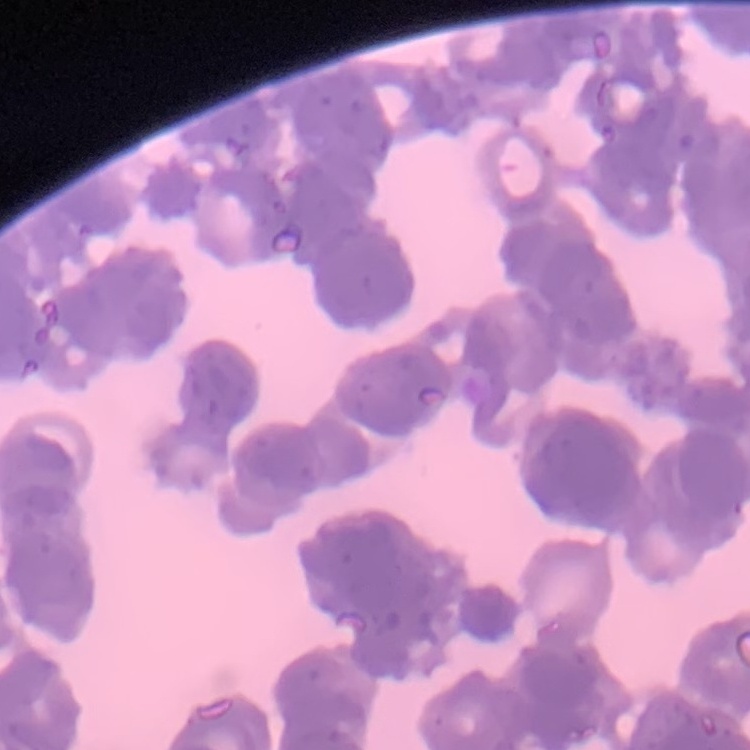

red blood cell morphology = rouleaux formation
stain = Field's or Giemsa
preparation = thin peripheral smear
image type = one tile cut from a larger photomicrograph